Identify the parasite.
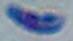
Toxoplasma gondii.

Micrograph. Captured at 1000x magnification.